Report the malaria status.
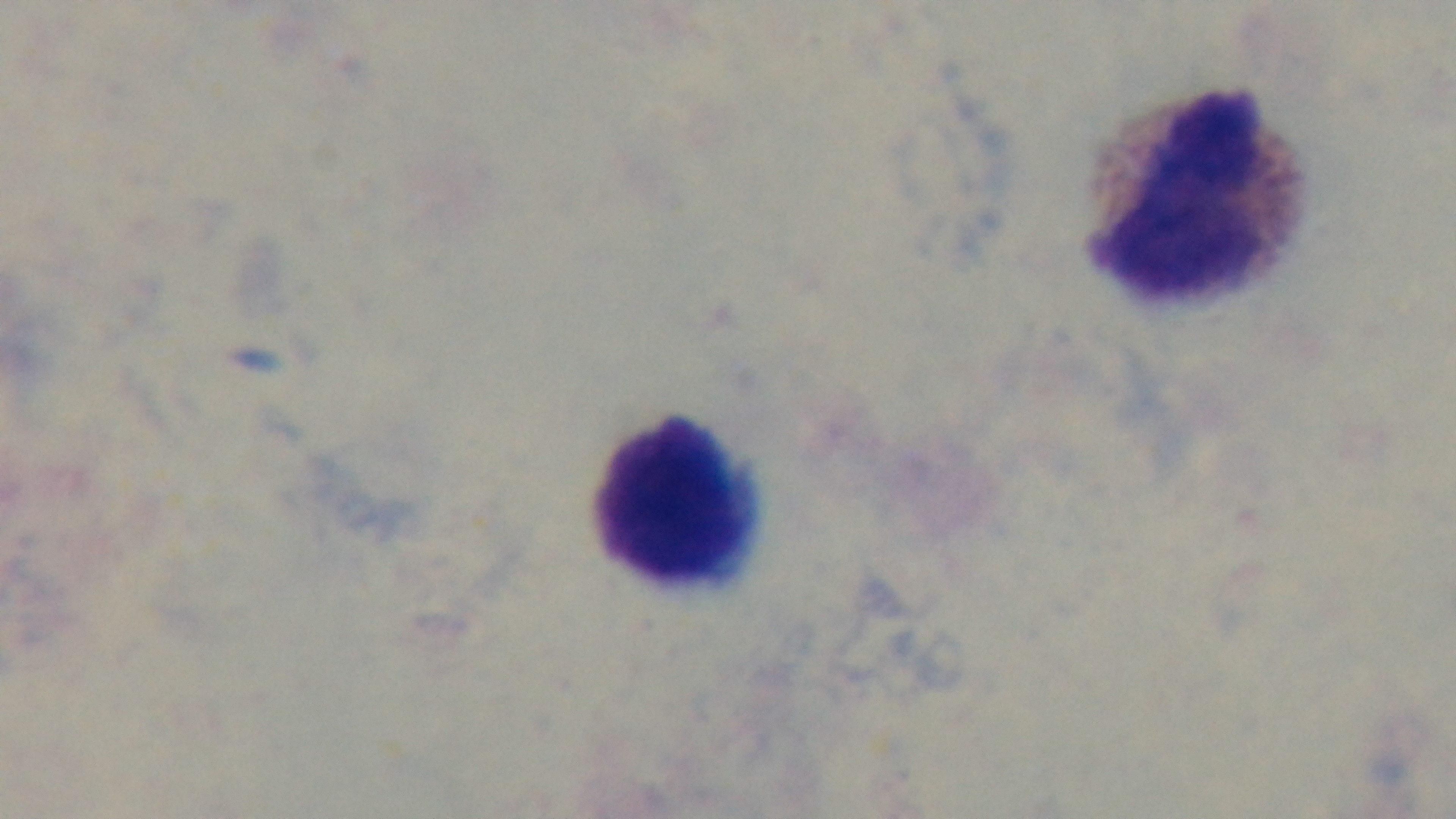
Uninfected.

Summary:
  - Objective: 100x oil immersion
  - Capture: mounted 4K digital camera
  - Stain: Giemsa
  - Preparation: thick smear
  - Field of view: single
  - Modality: light microscopy